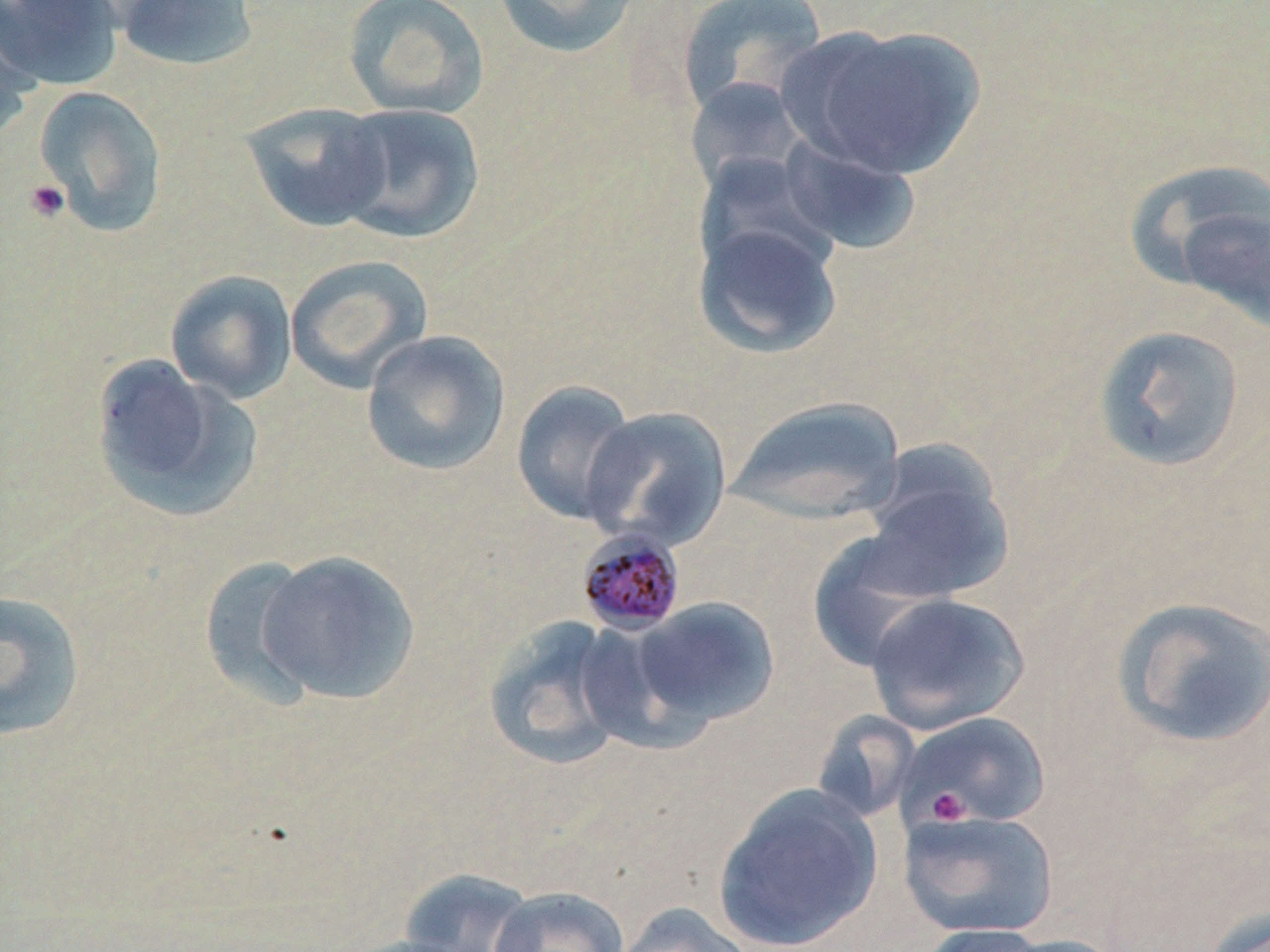

slide-level diagnosis = Plasmodium malariae
modality = optical microscopy
preparation = thin blood film
image size = 1270×952 pixels
Plasmodium malariae-infected red blood cell locations = approximate bounding boxes as named x1/y1/x2/y2 corners in pixels: (x1=575, y1=527, x2=687, y2=636)
field of view = single
platelet locations = approximate bounding boxes as named x1/y1/x2/y2 corners in pixels: (x1=24, y1=179, x2=71, y2=224), (x1=926, y1=787, x2=972, y2=826)
uninfected red blood cell locations = approximate bounding boxes as named x1/y1/x2/y2 corners in pixels: (x1=0, y1=0, x2=124, y2=91), (x1=112, y1=0, x2=261, y2=72), (x1=342, y1=0, x2=491, y2=119), (x1=493, y1=0, x2=643, y2=59), (x1=676, y1=1, x2=829, y2=120), (x1=0, y1=4, x2=44, y2=139), (x1=782, y1=23, x2=986, y2=180), (x1=683, y1=76, x2=812, y2=196), (x1=33, y1=85, x2=168, y2=237), (x1=240, y1=101, x2=392, y2=232), (x1=333, y1=103, x2=485, y2=244), (x1=775, y1=133, x2=921, y2=255), (x1=693, y1=152, x2=843, y2=281), (x1=1123, y1=159, x2=1269, y2=300), (x1=1174, y1=197, x2=1270, y2=336), (x1=693, y1=218, x2=843, y2=360), (x1=285, y1=254, x2=433, y2=394), (x1=165, y1=269, x2=298, y2=404), (x1=1093, y1=324, x2=1248, y2=473), (x1=360, y1=329, x2=511, y2=476), (x1=89, y1=354, x2=259, y2=522), (x1=511, y1=379, x2=641, y2=526), (x1=726, y1=395, x2=906, y2=526), (x1=580, y1=405, x2=732, y2=551), (x1=856, y1=450, x2=1015, y2=602), (x1=807, y1=532, x2=951, y2=672), (x1=253, y1=549, x2=423, y2=706), (x1=198, y1=555, x2=325, y2=708), (x1=0, y1=589, x2=88, y2=743), (x1=864, y1=591, x2=1031, y2=734), (x1=1111, y1=596, x2=1270, y2=750), (x1=629, y1=597, x2=781, y2=731), (x1=481, y1=615, x2=634, y2=771), (x1=897, y1=710, x2=1052, y2=829), (x1=710, y1=783, x2=884, y2=952), (x1=898, y1=808, x2=1059, y2=940), (x1=394, y1=868, x2=543, y2=952), (x1=487, y1=886, x2=630, y2=952), (x1=611, y1=903, x2=757, y2=952), (x1=1201, y1=906, x2=1270, y2=952), (x1=910, y1=924, x2=1065, y2=951), (x1=984, y1=933, x2=1131, y2=952)
stain = May-Grünwald-Giemsa
magnification = 1000x